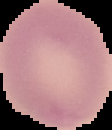
preparation: thin blood smear
malaria_status: uninfected
image_size: 112×130 pixels
image_type: segmented cell region with the area outside set to black